Locate every blood parasite and identify its species.
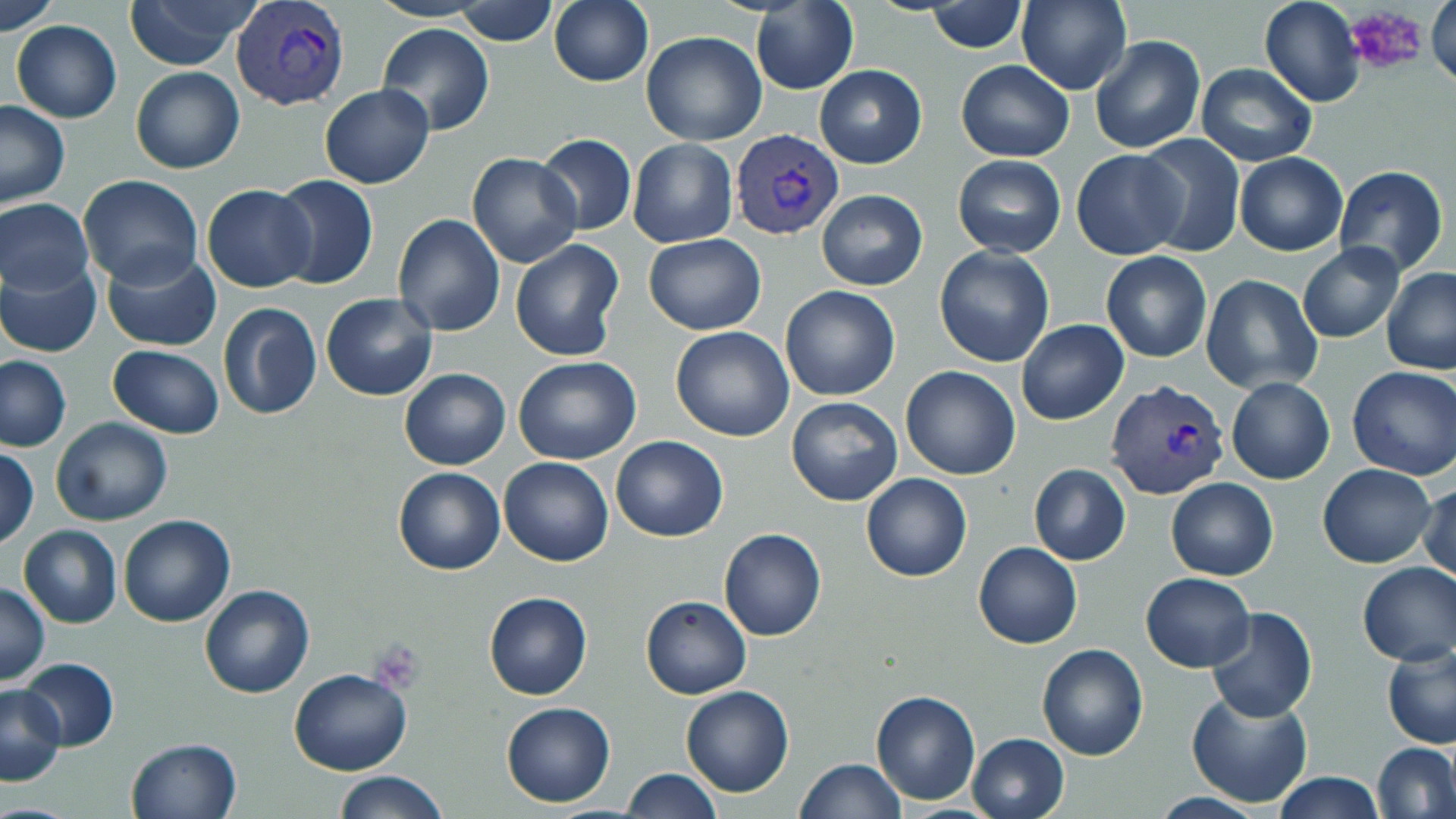
Approximate bounding boxes as named x1/y1/x2/y2 corners in pixels.
Plasmodium vivax-infected red blood cells: (x1=228, y1=2, x2=349, y2=112), (x1=729, y1=129, x2=846, y2=241), (x1=1107, y1=378, x2=1232, y2=501).
No Plasmodium falciparum, Plasmodium ovale, Plasmodium malariae, Babesia divergens, or Trypanosoma brucei observed.

Summary:
  - Uninfected red blood cell locations: (x1=1, y1=0, x2=62, y2=33), (x1=122, y1=0, x2=261, y2=70), (x1=454, y1=0, x2=557, y2=46), (x1=1017, y1=0, x2=1130, y2=94), (x1=1260, y1=0, x2=1364, y2=107), (x1=1427, y1=0, x2=1456, y2=93), (x1=548, y1=1, x2=653, y2=87), (x1=927, y1=2, x2=1029, y2=54), (x1=751, y1=3, x2=858, y2=94), (x1=11, y1=21, x2=122, y2=121), (x1=376, y1=23, x2=495, y2=134), (x1=640, y1=31, x2=766, y2=145), (x1=1090, y1=35, x2=1205, y2=154), (x1=954, y1=60, x2=1074, y2=162), (x1=1196, y1=63, x2=1317, y2=166), (x1=812, y1=64, x2=926, y2=167), (x1=131, y1=67, x2=244, y2=174), (x1=319, y1=84, x2=434, y2=189), (x1=0, y1=99, x2=70, y2=207), (x1=535, y1=134, x2=636, y2=235), (x1=1137, y1=134, x2=1246, y2=256), (x1=627, y1=139, x2=737, y2=248), (x1=1071, y1=149, x2=1188, y2=260), (x1=1234, y1=152, x2=1347, y2=256), (x1=465, y1=153, x2=583, y2=269), (x1=951, y1=156, x2=1067, y2=258), (x1=1333, y1=165, x2=1449, y2=275), (x1=78, y1=175, x2=203, y2=288), (x1=270, y1=175, x2=377, y2=290), (x1=202, y1=184, x2=316, y2=293), (x1=816, y1=189, x2=928, y2=291), (x1=1, y1=199, x2=94, y2=294), (x1=392, y1=213, x2=504, y2=336), (x1=643, y1=235, x2=765, y2=335), (x1=510, y1=238, x2=625, y2=361), (x1=1296, y1=243, x2=1404, y2=344), (x1=933, y1=247, x2=1055, y2=367), (x1=102, y1=248, x2=221, y2=351), (x1=1100, y1=249, x2=1213, y2=362), (x1=0, y1=258, x2=101, y2=358), (x1=1381, y1=268, x2=1456, y2=375), (x1=1200, y1=275, x2=1323, y2=394), (x1=780, y1=285, x2=900, y2=401), (x1=321, y1=294, x2=438, y2=401), (x1=218, y1=302, x2=321, y2=420), (x1=1016, y1=320, x2=1129, y2=425), (x1=670, y1=326, x2=795, y2=442), (x1=108, y1=345, x2=224, y2=438), (x1=0, y1=355, x2=73, y2=453), (x1=513, y1=356, x2=641, y2=465), (x1=1348, y1=365, x2=1456, y2=480), (x1=900, y1=366, x2=1020, y2=479), (x1=399, y1=368, x2=510, y2=471), (x1=1226, y1=377, x2=1334, y2=485), (x1=786, y1=395, x2=903, y2=506), (x1=51, y1=417, x2=173, y2=527), (x1=610, y1=435, x2=728, y2=541), (x1=1, y1=447, x2=39, y2=549), (x1=499, y1=456, x2=613, y2=566), (x1=1317, y1=463, x2=1437, y2=567), (x1=1028, y1=464, x2=1130, y2=566), (x1=393, y1=467, x2=505, y2=576), (x1=860, y1=472, x2=971, y2=582), (x1=1166, y1=477, x2=1278, y2=581), (x1=1417, y1=481, x2=1455, y2=585), (x1=118, y1=514, x2=235, y2=627), (x1=18, y1=525, x2=121, y2=629), (x1=719, y1=528, x2=826, y2=641), (x1=973, y1=542, x2=1082, y2=650), (x1=1356, y1=561, x2=1456, y2=666), (x1=1139, y1=572, x2=1255, y2=672), (x1=0, y1=580, x2=50, y2=684), (x1=200, y1=584, x2=314, y2=699), (x1=483, y1=591, x2=593, y2=702), (x1=641, y1=595, x2=751, y2=699), (x1=1204, y1=606, x2=1317, y2=724), (x1=1036, y1=642, x2=1148, y2=760), (x1=1382, y1=642, x2=1456, y2=750), (x1=17, y1=657, x2=118, y2=752), (x1=288, y1=668, x2=412, y2=775), (x1=0, y1=683, x2=66, y2=786), (x1=680, y1=686, x2=795, y2=797), (x1=1185, y1=688, x2=1312, y2=808), (x1=869, y1=689, x2=981, y2=806), (x1=501, y1=701, x2=616, y2=806), (x1=966, y1=733, x2=1069, y2=819), (x1=125, y1=737, x2=242, y2=819), (x1=1373, y1=742, x2=1456, y2=819), (x1=794, y1=758, x2=905, y2=818), (x1=620, y1=768, x2=721, y2=817), (x1=330, y1=770, x2=451, y2=819), (x1=1273, y1=772, x2=1384, y2=818)
  - Platelet locations: (x1=1345, y1=6, x2=1427, y2=73), (x1=369, y1=641, x2=424, y2=692)
  - Slide-level diagnosis: Plasmodium vivax
  - Modality: light microscopy
  - Image size: 1456×819 pixels
  - Magnification: 1000x
  - Field of view: one of a larger specimen
  - Preparation: thin blood film
  - Stain: May-Grünwald-Giemsa